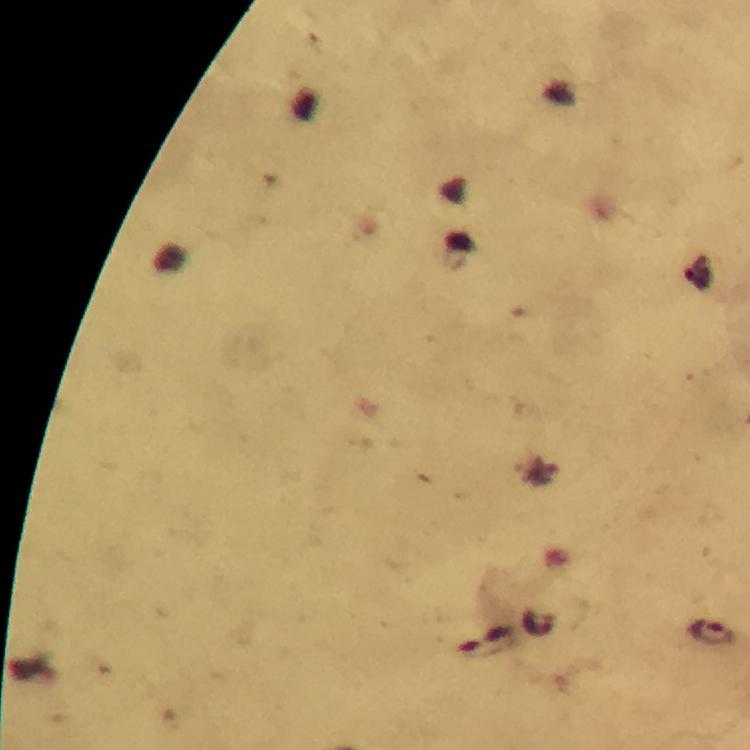 Approximate centers as (x, y) in pixels. Malaria parasite locations: (538, 623), (713, 632). Giemsa-stained preparation. Immersion oil applied. Photographed through the microscope with a smartphone camera. 100x magnification. Image is 750×750 pixels. From a diagnostic examination for malaria. Thick blood smear. A crop from one field of view.